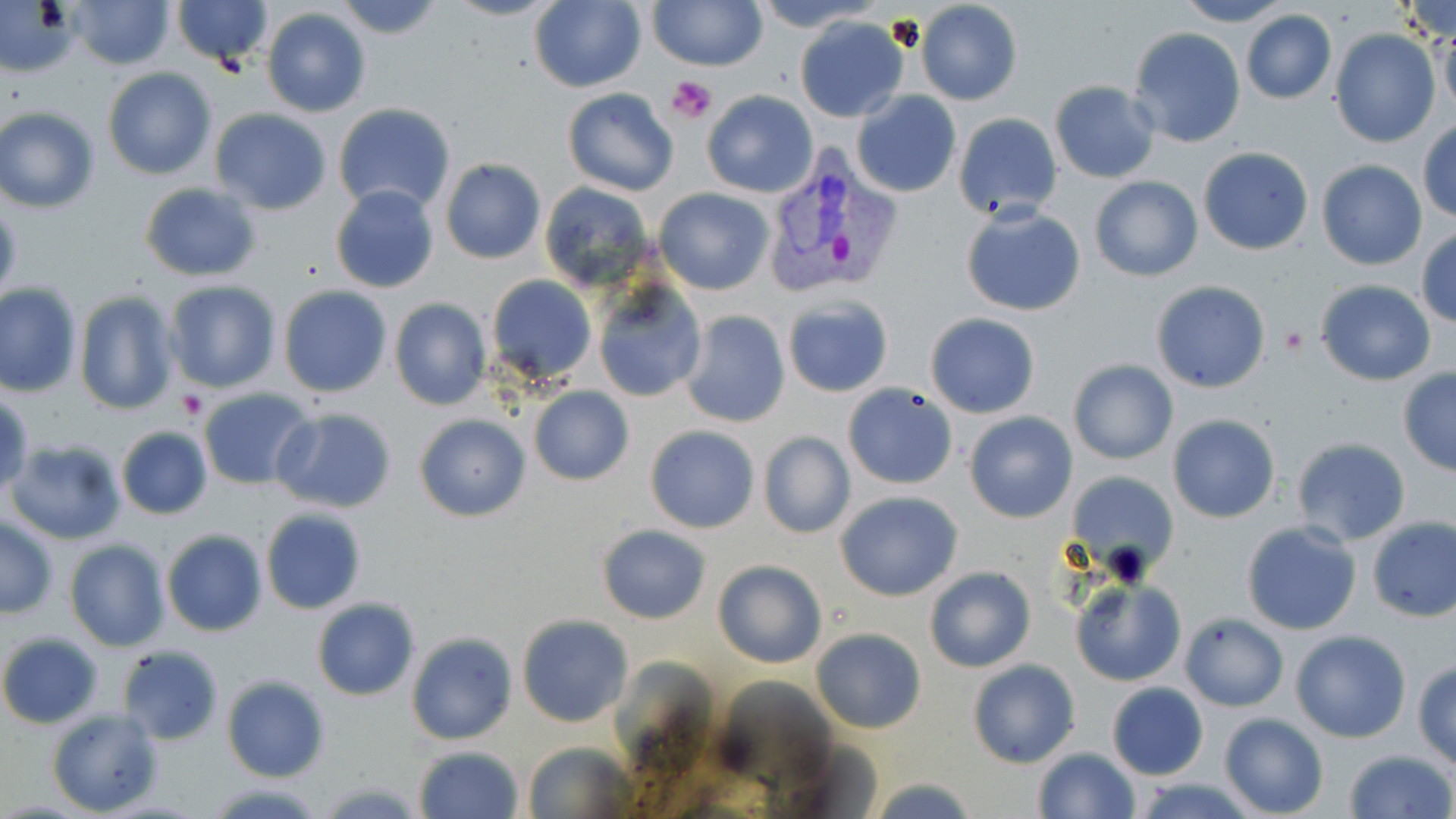 Approximate bounding boxes as (x1, y1, x2, y2) in pixels. Uninfected red blood cell locations: (331, 0, 444, 40), (444, 0, 561, 21), (648, 0, 765, 70), (750, 0, 880, 29), (1173, 0, 1293, 26), (1400, 0, 1456, 50), (66, 1, 175, 70), (171, 1, 275, 69), (531, 1, 646, 93), (915, 2, 1023, 106), (261, 7, 372, 118), (1240, 11, 1336, 104), (794, 15, 909, 122), (1436, 22, 1456, 121), (1129, 27, 1247, 148), (1331, 29, 1440, 147), (102, 67, 216, 180), (1049, 82, 1160, 183), (564, 88, 679, 197), (701, 91, 817, 197), (852, 91, 960, 198), (332, 104, 456, 217), (0, 106, 101, 213), (209, 110, 332, 215), (953, 112, 1062, 223), (1417, 119, 1455, 223), (1198, 147, 1315, 256), (439, 158, 546, 265), (1316, 160, 1427, 270), (1089, 175, 1203, 281), (540, 181, 656, 292), (139, 182, 262, 280), (329, 185, 441, 297), (654, 188, 773, 294), (0, 197, 22, 308), (961, 204, 1085, 317), (1414, 226, 1456, 328), (486, 274, 596, 386), (163, 279, 281, 393), (1150, 280, 1271, 393), (1314, 280, 1434, 385), (0, 282, 83, 397), (594, 283, 707, 403), (277, 285, 392, 398), (74, 291, 179, 416), (781, 295, 893, 398), (389, 299, 491, 411), (682, 311, 790, 427), (925, 314, 1039, 419), (1068, 359, 1178, 465), (1397, 368, 1456, 476), (842, 383, 959, 490), (528, 386, 634, 486), (198, 389, 316, 491), (0, 391, 32, 501), (273, 408, 398, 512), (964, 411, 1078, 523), (414, 413, 530, 522), (1168, 414, 1280, 523), (115, 426, 213, 521), (645, 426, 760, 532), (758, 431, 856, 539), (1290, 436, 1412, 545), (6, 438, 126, 544), (1066, 471, 1179, 581), (835, 491, 963, 601), (260, 508, 366, 615), (0, 516, 57, 618), (1365, 517, 1456, 623), (159, 521, 364, 625), (1241, 522, 1363, 635), (597, 525, 710, 623), (161, 530, 267, 637), (64, 538, 172, 653), (713, 561, 827, 668), (923, 566, 1036, 674), (1070, 579, 1186, 686), (312, 598, 419, 700), (1180, 612, 1288, 711), (517, 614, 633, 727), (811, 628, 927, 733), (1291, 630, 1411, 742), (0, 632, 104, 729), (407, 632, 517, 745), (117, 645, 224, 745), (968, 660, 1079, 768), (1413, 660, 1456, 769), (221, 676, 330, 782), (1106, 683, 1208, 779), (46, 708, 163, 816), (1218, 713, 1328, 819), (521, 742, 639, 817), (413, 745, 523, 819), (1032, 747, 1139, 818), (1341, 749, 1454, 819), (865, 777, 983, 817), (1132, 778, 1253, 819), (315, 780, 425, 816), (205, 781, 328, 819). Platelet locations: (667, 76, 716, 123), (1278, 324, 1309, 357), (176, 390, 208, 421). Plasmodium vivax-infected red blood cell locations: (758, 147, 903, 301). Slide-level diagnosis: Plasmodium vivax. May-Grünwald-Giemsa-stained preparation. Captured at 1000x magnification. Thin blood smear. Light microscopy. One field of a larger specimen. Image is 1456×819 pixels.